Assess this cell for malaria.
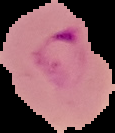

It is parasitized.

image type = segmented cell region with the area outside set to black
preparation = thin blood film
image size = 115×133 pixels